Classify this cell by malaria status.
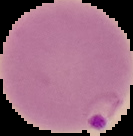

It is parasitized.

preparation: thin blood film
image_size: 133×136 pixels
image_type: segmented cell region on a black background